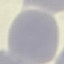
Summary:
  - Result: no malaria parasites detected
  - Capture: smartphone through the microscope eyepiece
  - Stain: Giemsa
  - Image type: automatically extracted cell patch, resized to 64 × 64 pixels
  - Preparation: thin smear